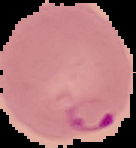

image size = 136×148 pixels
preparation = thin blood film
image type = segmented cell region with the area outside set to black
malaria status = parasitized